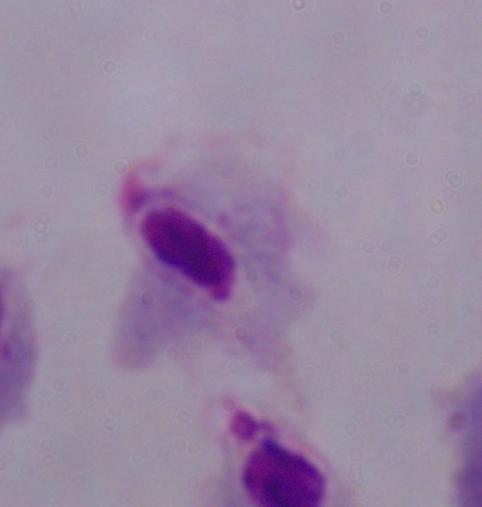

A trichomonad is seen. Photomicrograph. 1000x magnification.